Report the malaria status of this cell.
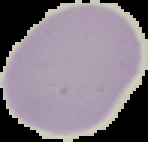

It is uninfected.

image size = 148×142 pixels
image type = segmented cell region on a black background
preparation = thin blood film